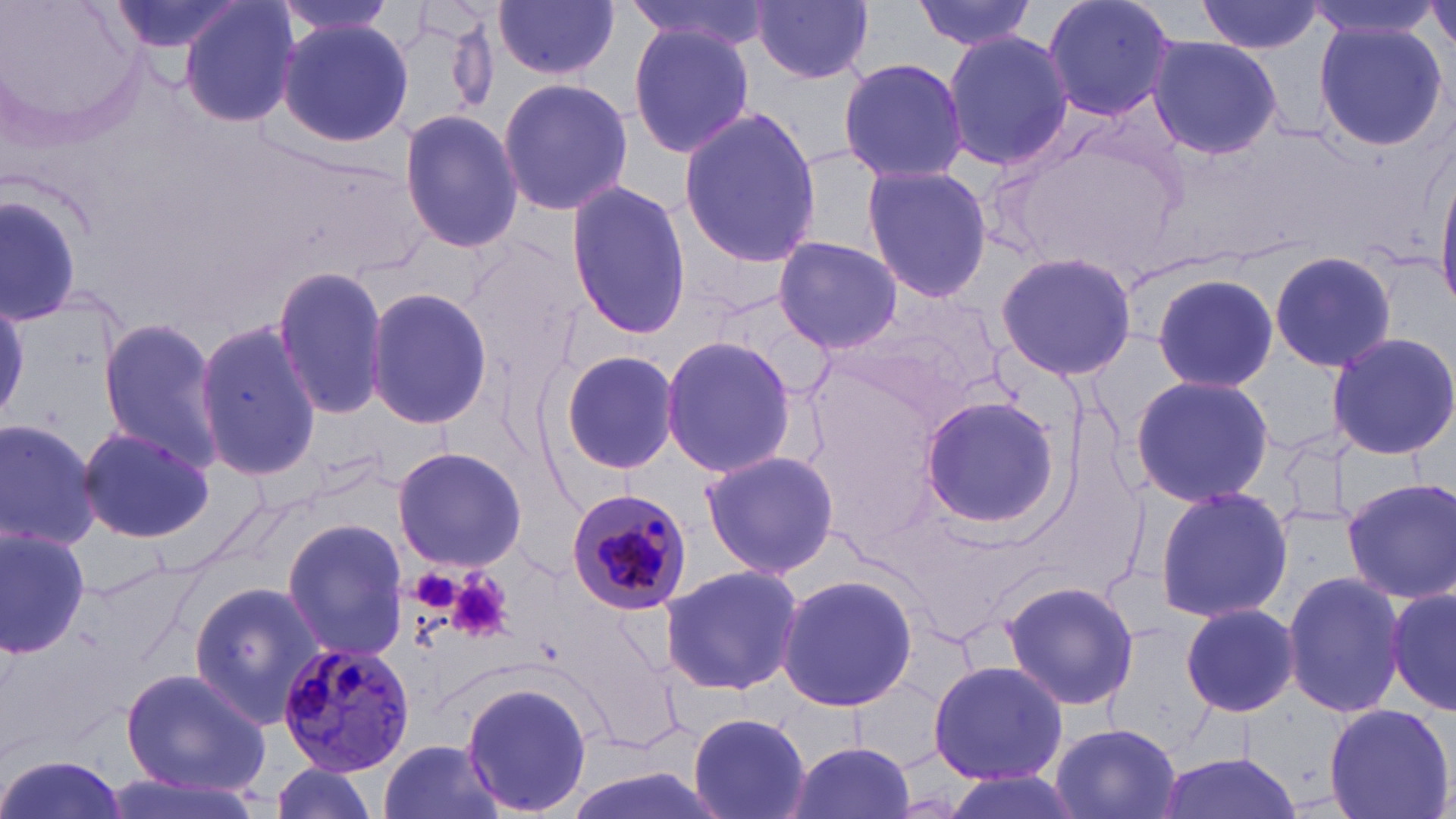
Summary:
  - Coordinate format: approximate bounding boxes as (x1,y1)-(x2,y2) corner pairs in pixels
  - Uninfected red blood cell locations: (1,0)-(153,150), (103,0)-(250,57), (178,0)-(300,127), (272,0)-(404,37), (627,0)-(771,54), (748,0)-(876,84), (912,0)-(1038,52), (1042,0)-(1177,122), (1196,0)-(1322,55), (1308,0)-(1438,44), (494,1)-(619,80), (1427,1)-(1456,54), (276,17)-(413,149), (1313,23)-(1452,152), (629,24)-(755,157), (942,30)-(1073,172), (1142,34)-(1283,162), (838,57)-(968,183), (496,77)-(633,216), (678,106)-(823,268), (399,107)-(522,253), (861,161)-(993,303), (1434,169)-(1456,310), (564,181)-(693,339), (1,188)-(86,327), (774,237)-(902,353), (1267,248)-(1399,376), (994,250)-(1137,382), (272,264)-(392,423), (1150,273)-(1281,391), (365,286)-(492,432), (0,294)-(31,419), (97,316)-(222,471), (193,317)-(323,484), (1323,331)-(1456,462), (659,336)-(800,480), (556,350)-(681,477), (1128,374)-(1276,507), (919,395)-(1063,529), (0,414)-(101,553), (75,426)-(216,543), (392,446)-(527,572), (701,450)-(841,578), (1341,476)-(1456,604), (1153,487)-(1293,623), (281,519)-(407,660), (0,527)-(92,658), (661,563)-(807,696), (1283,569)-(1408,716), (774,571)-(919,714), (1001,579)-(1139,712), (1386,581)-(1455,719), (190,582)-(328,728), (1180,603)-(1301,717), (927,658)-(1066,788), (119,667)-(270,797), (461,679)-(593,818), (1322,702)-(1453,819), (687,709)-(812,819), (1048,722)-(1182,819), (785,738)-(913,818), (377,739)-(507,819), (1151,751)-(1303,819), (0,753)-(127,819), (264,763)-(382,819), (102,769)-(269,819)
  - Platelet locations: (448,570)-(512,641)
  - Plasmodium malariae-infected red blood cell locations: (562,484)-(695,615), (277,640)-(417,777)
  - Slide-level diagnosis: Plasmodium malariae
  - Modality: light microscopy
  - Field of view: single
  - Magnification: 1000x
  - Stain: May-Grünwald-Giemsa
  - Preparation: thin blood smear
  - Image size: 1456×819 pixels